Locate every Trypanosoma brucei.
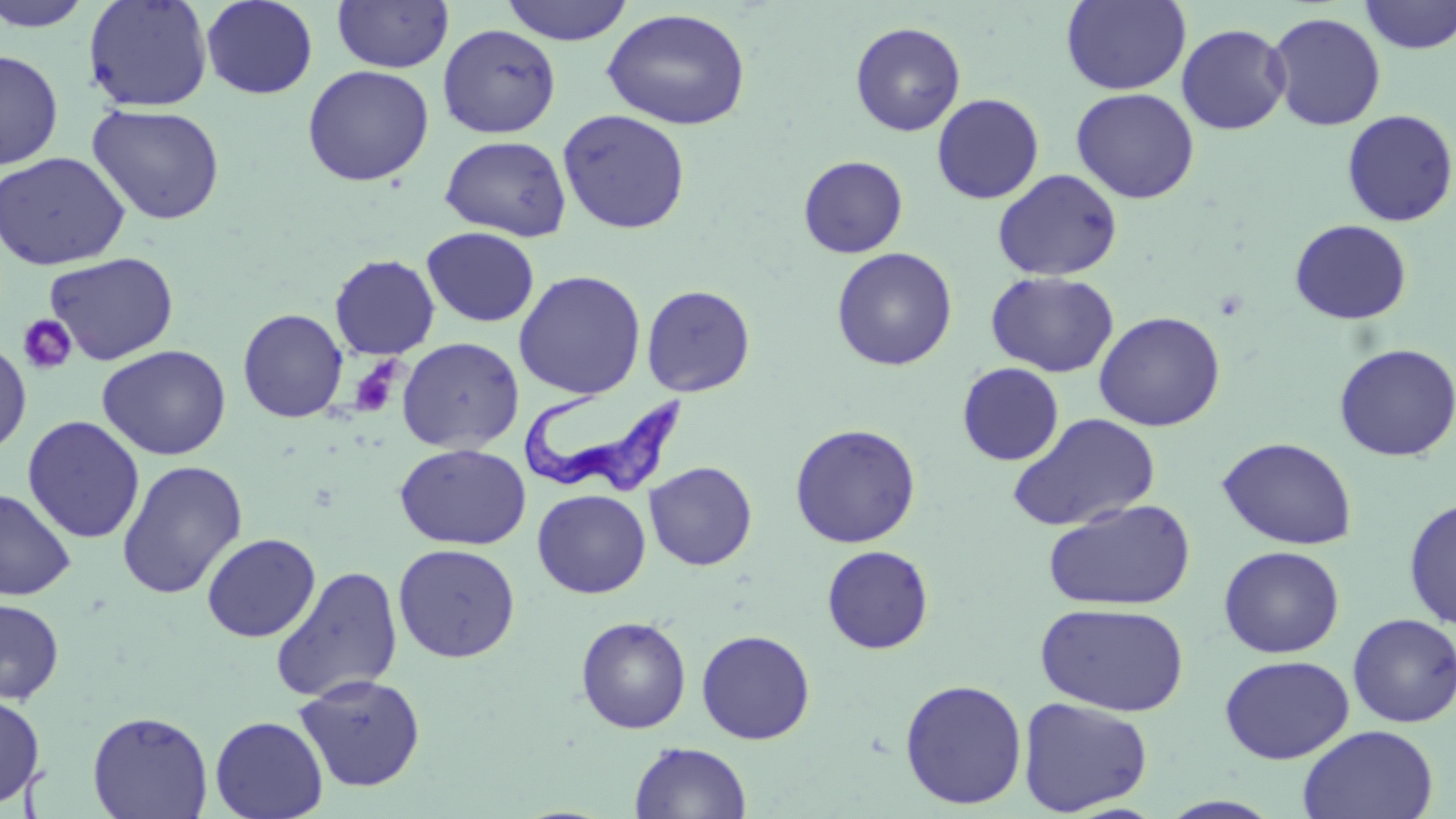

Approximate bounding boxes as (x1,y1)-(x2,y2) corner pairs in pixels.
Trypanosoma brucei: (521,391)-(692,500).

Summary:
  - Uninfected red blood cell locations: (0,0)-(94,32), (83,0)-(213,113), (201,0)-(318,99), (332,0)-(453,73), (500,0)-(634,45), (1360,0)-(1456,54), (1060,1)-(1192,95), (601,8)-(751,131), (1266,11)-(1386,132), (850,21)-(966,136), (1176,23)-(1291,135), (437,24)-(561,138), (0,49)-(63,169), (302,65)-(434,187), (1070,88)-(1200,204), (931,93)-(1044,205), (87,103)-(226,225), (557,109)-(690,234), (1341,109)-(1455,227), (440,135)-(571,241), (0,152)-(131,270), (798,155)-(908,258), (992,169)-(1122,281), (1289,219)-(1412,325), (422,226)-(539,327), (831,247)-(958,371), (44,252)-(179,365), (329,254)-(440,360), (513,270)-(646,399), (986,270)-(1119,378), (640,284)-(756,397), (238,308)-(348,423), (1093,311)-(1226,432), (0,337)-(32,456), (396,337)-(525,453), (1333,342)-(1456,462), (96,344)-(231,461), (957,362)-(1064,465), (1007,413)-(1161,532), (23,416)-(145,543), (789,423)-(921,548), (1217,437)-(1357,550), (395,443)-(531,550), (116,460)-(248,599), (644,461)-(757,571), (0,486)-(76,601), (532,489)-(651,598), (1042,498)-(1196,611), (1403,498)-(1456,630), (201,533)-(321,642), (393,543)-(520,663), (822,545)-(934,654), (1218,545)-(1345,658), (270,565)-(403,703), (0,598)-(64,704), (1035,602)-(1189,717), (1347,613)-(1456,727), (575,616)-(691,734), (696,629)-(816,744), (1219,654)-(1355,765), (293,673)-(426,792), (899,678)-(1027,810), (0,693)-(45,809), (1017,696)-(1153,816), (87,710)-(213,819), (210,715)-(328,819), (1298,725)-(1439,818), (629,741)-(752,818)
  - Platelet locations: (18,314)-(78,375), (349,363)-(400,420)
  - Slide-level diagnosis: Trypanosoma brucei
  - Stain: May-Grünwald-Giemsa
  - Preparation: thin blood smear
  - Image size: 1456×819 pixels
  - Modality: optical microscopy
  - Magnification: 1000x
  - Field of view: single